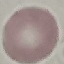

result: no malaria parasites seen
preparation: thin smear
image_type: cell patch, automatically extracted from a larger field of view and resized to 64 × 64 pixels
stain: Giemsa
capture: smartphone through the microscope eyepiece